Give the position of every Plasmodium parasite.
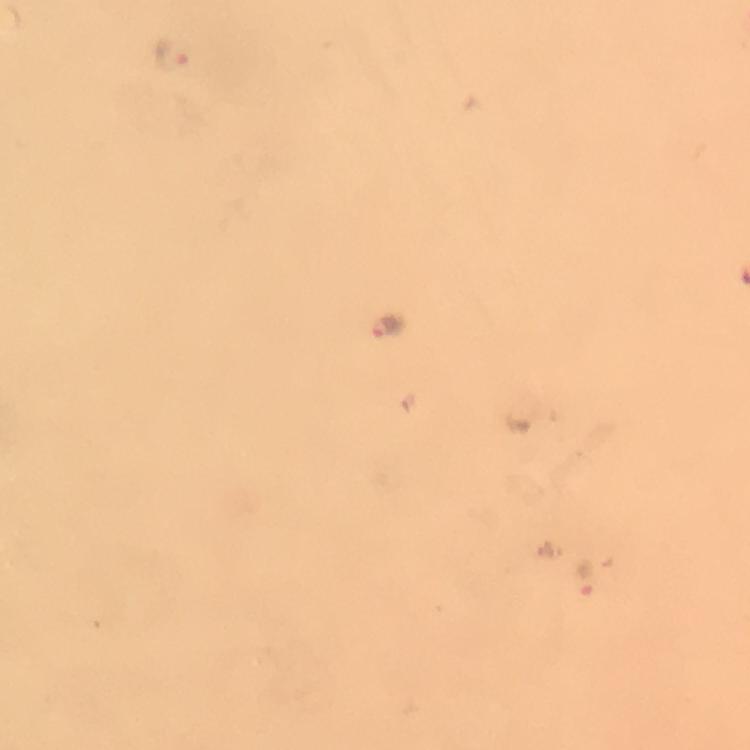

Approximate object centers, in pixels from the top-left corner.
Plasmodium parasites: (x=172, y=57), (x=386, y=326).

Summary:
  - Context: from a diagnostic examination for malaria
  - Immersion oil: applied
  - Magnification: 100x
  - Stain: Giemsa
  - Cropped from: a single field of view
  - Image size: 750×750 pixels
  - Preparation: thick blood film
  - Capture: smartphone photograph through a microscope